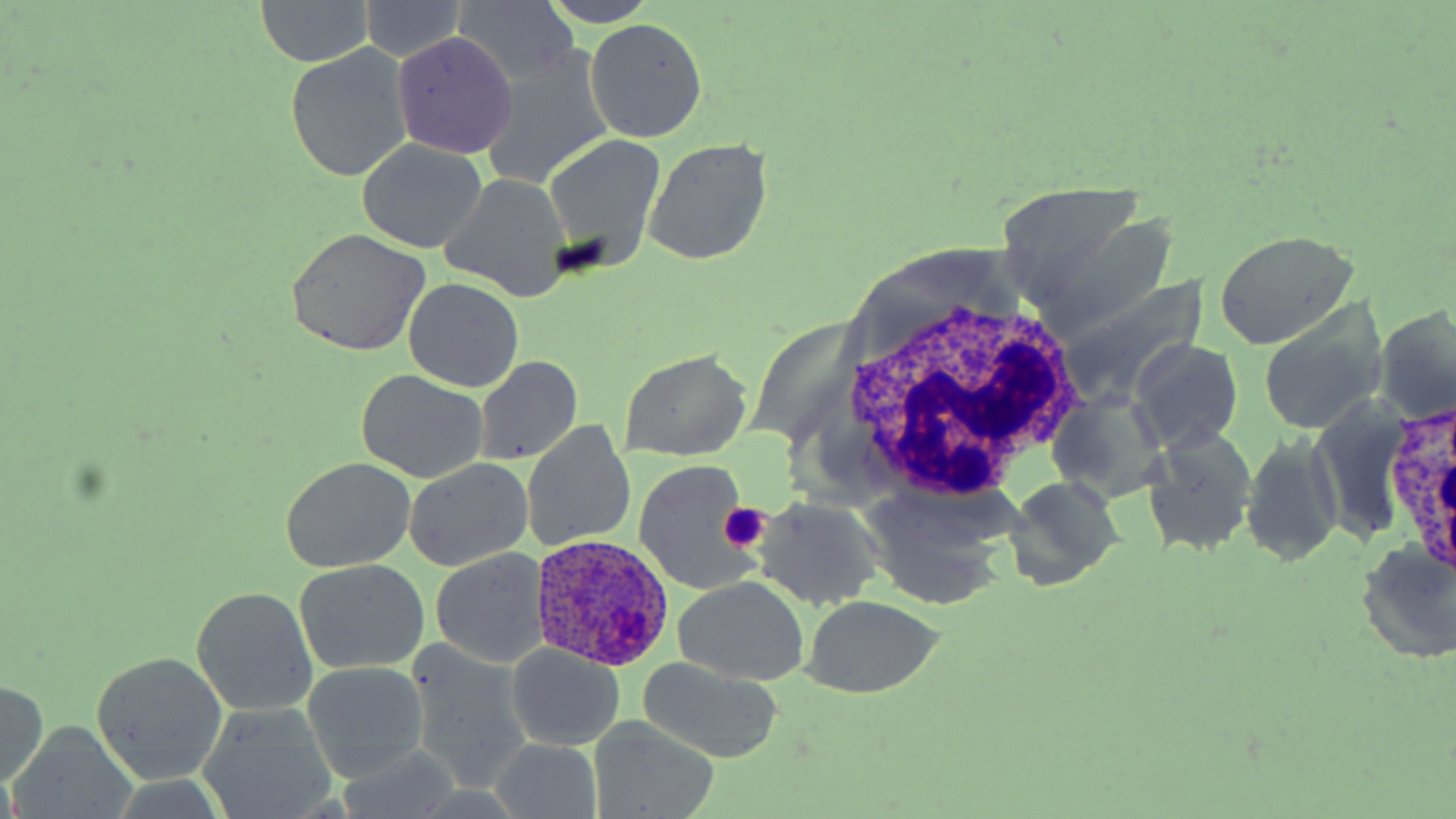
slide-level diagnosis = Plasmodium ovale
uninfected red blood cell locations = approximate bounding boxes as (x1, y1, x2, y2) in pixels: (537, 0, 662, 26), (251, 1, 381, 67), (359, 2, 470, 65), (449, 2, 580, 86), (586, 18, 707, 144), (392, 32, 517, 159), (286, 44, 414, 183), (481, 47, 618, 186), (543, 134, 668, 269), (357, 139, 488, 253), (644, 139, 771, 264), (441, 174, 572, 302), (284, 228, 431, 355), (1213, 231, 1358, 349), (403, 278, 524, 393), (1256, 301, 1389, 436), (1376, 304, 1456, 427), (1128, 339, 1243, 454), (619, 349, 753, 462), (475, 355, 583, 466), (358, 370, 487, 483), (1048, 388, 1169, 503), (1307, 396, 1417, 547), (522, 421, 638, 552), (1143, 426, 1259, 557), (1241, 430, 1343, 568), (280, 457, 416, 572), (404, 458, 533, 572), (633, 459, 761, 595), (1003, 474, 1124, 591), (855, 485, 1016, 613), (750, 497, 887, 611), (1355, 539, 1453, 664), (431, 548, 548, 669), (294, 559, 429, 676), (672, 578, 809, 687), (191, 585, 317, 715), (800, 596, 944, 699), (404, 640, 534, 793), (505, 646, 626, 749), (89, 652, 228, 785), (636, 657, 785, 765), (302, 660, 428, 782), (0, 680, 49, 787), (200, 705, 337, 817), (588, 718, 720, 818), (9, 723, 131, 819), (491, 738, 604, 817)
modality = optical microscopy
Plasmodium ovale-infected red blood cell locations = approximate bounding boxes as (x1, y1, x2, y2) in pixels: (529, 538, 674, 672)
preparation = thin blood film
field of view = single
stain = May-Grünwald-Giemsa
platelet locations = approximate bounding boxes as (x1, y1, x2, y2) in pixels: (718, 501, 770, 551)
magnification = 1000x
image size = 1456×819 pixels
white blood cell locations = approximate bounding boxes as (x1, y1, x2, y2) in pixels: (837, 286, 1085, 505), (1385, 402, 1456, 572)